Name the cell type shown.
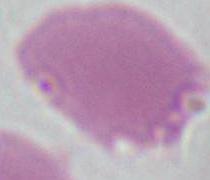
This is an erythrocyte.

1000x magnification. Micrograph.